Locate every blood parasite and identify its species.
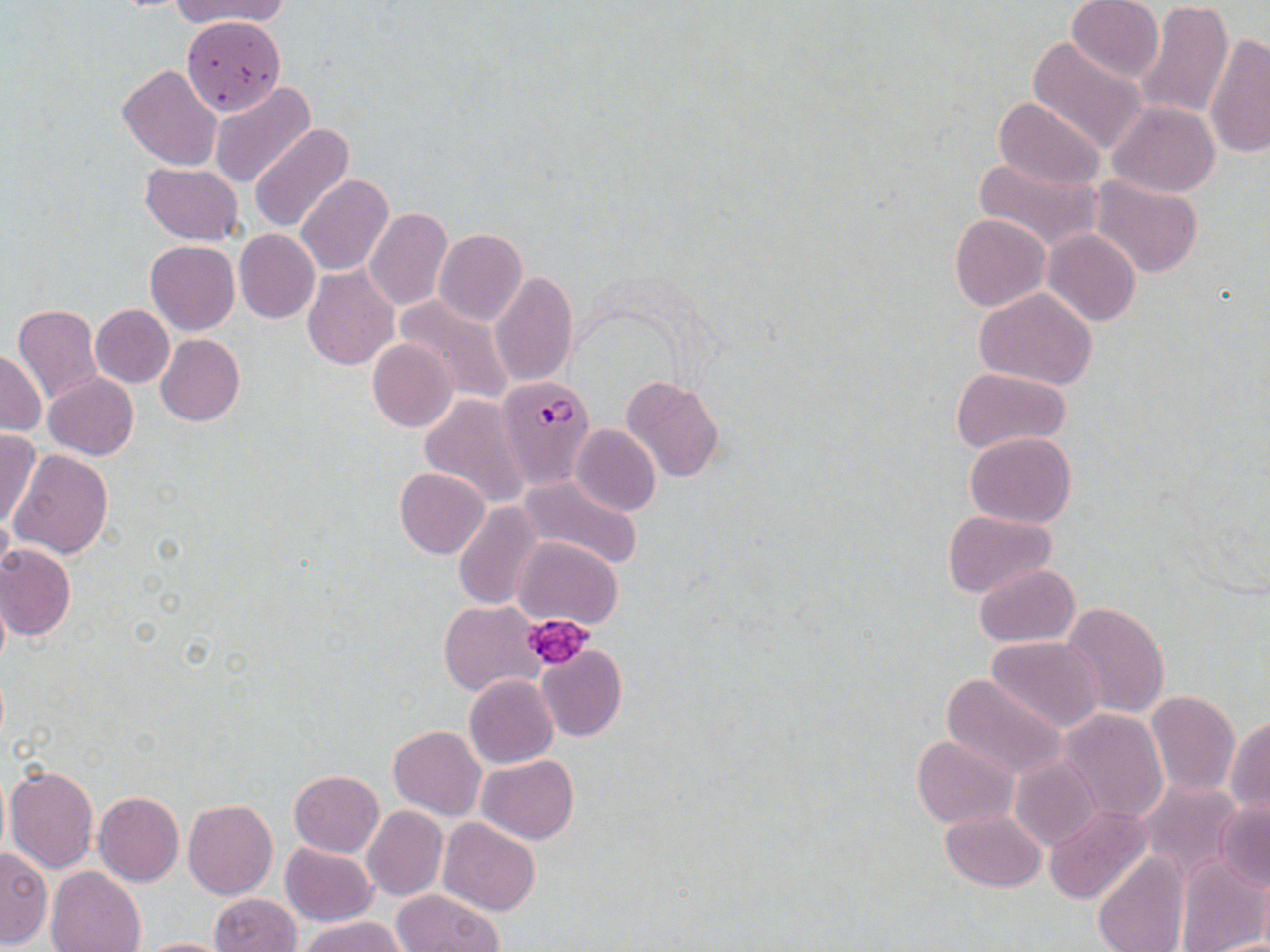

Approximate bounding boxes as (x1, y1, x2, y2) in pixels.
Plasmodium falciparum-infected red blood cells: (496, 373, 597, 489).
No Plasmodium ovale, Plasmodium malariae, Plasmodium vivax, Babesia divergens, or Trypanosoma brucei observed.

slide-level diagnosis = Plasmodium falciparum
magnification = 1000x
platelet locations = approximate bounding boxes as (x1, y1, x2, y2) in pixels: (523, 613, 594, 672)
stain = May-Grünwald-Giemsa
uninfected red blood cell locations = approximate bounding boxes as (x1, y1, x2, y2) in pixels: (168, 0, 291, 28), (1066, 0, 1164, 85), (1133, 0, 1233, 119), (180, 17, 289, 117), (1205, 35, 1270, 157), (1027, 38, 1149, 154), (117, 64, 222, 171), (209, 81, 316, 190), (993, 96, 1105, 192), (1107, 100, 1220, 197), (249, 123, 354, 233), (972, 154, 1104, 255), (140, 163, 243, 244), (296, 175, 395, 278), (1091, 176, 1204, 279), (364, 206, 453, 311), (950, 213, 1051, 312), (234, 229, 320, 323), (434, 229, 527, 327), (1042, 229, 1140, 327), (146, 240, 239, 335), (443, 246, 553, 367), (302, 264, 400, 371), (490, 271, 579, 387), (973, 289, 1098, 390), (391, 294, 515, 404), (90, 303, 174, 388), (13, 305, 103, 404), (155, 333, 244, 426), (367, 337, 456, 432), (0, 349, 46, 436), (951, 367, 1070, 452), (43, 373, 139, 461), (620, 375, 725, 484), (420, 394, 529, 509), (570, 425, 660, 516), (0, 428, 43, 528), (964, 430, 1077, 528), (9, 448, 113, 559), (394, 467, 489, 559), (517, 473, 644, 570), (454, 501, 544, 612), (943, 509, 1057, 598), (512, 536, 622, 628), (1, 544, 76, 640), (973, 563, 1080, 647), (0, 580, 11, 676), (440, 601, 542, 696), (1061, 602, 1170, 719), (985, 636, 1104, 732), (536, 645, 626, 742), (940, 672, 1068, 782), (465, 674, 558, 768), (1145, 690, 1240, 798), (1058, 709, 1168, 824), (1227, 715, 1270, 819), (389, 724, 486, 820), (912, 734, 1018, 828), (1010, 754, 1103, 851), (476, 755, 579, 843), (4, 762, 100, 874), (289, 770, 384, 857), (1140, 781, 1246, 885), (95, 792, 185, 885), (1212, 796, 1270, 893), (183, 798, 277, 899), (1044, 805, 1153, 904), (361, 806, 447, 901), (942, 809, 1046, 891), (438, 817, 540, 916), (280, 843, 376, 926), (1, 848, 52, 947), (1092, 850, 1190, 952), (1177, 854, 1268, 952), (44, 867, 147, 952), (392, 890, 504, 951), (210, 893, 301, 952), (300, 916, 406, 952), (129, 936, 238, 952)
preparation = thin blood film
field of view = single
image size = 1270×952 pixels
modality = light microscopy